Assess the morphology of the erythrocytes.
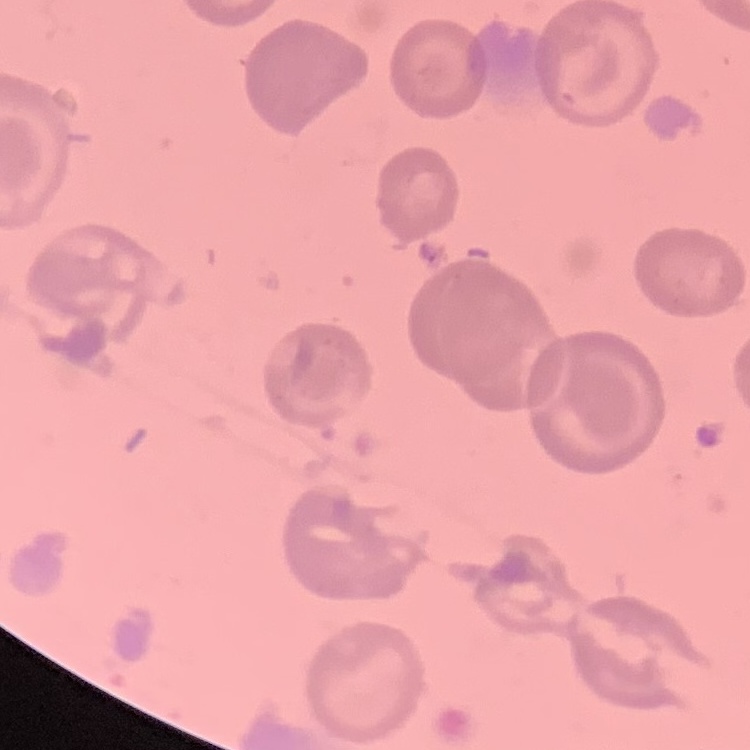
No rouleaux formation.

Thin peripheral smear. Stained with either Field's or Giemsa. One tile cut from a larger photomicrograph.